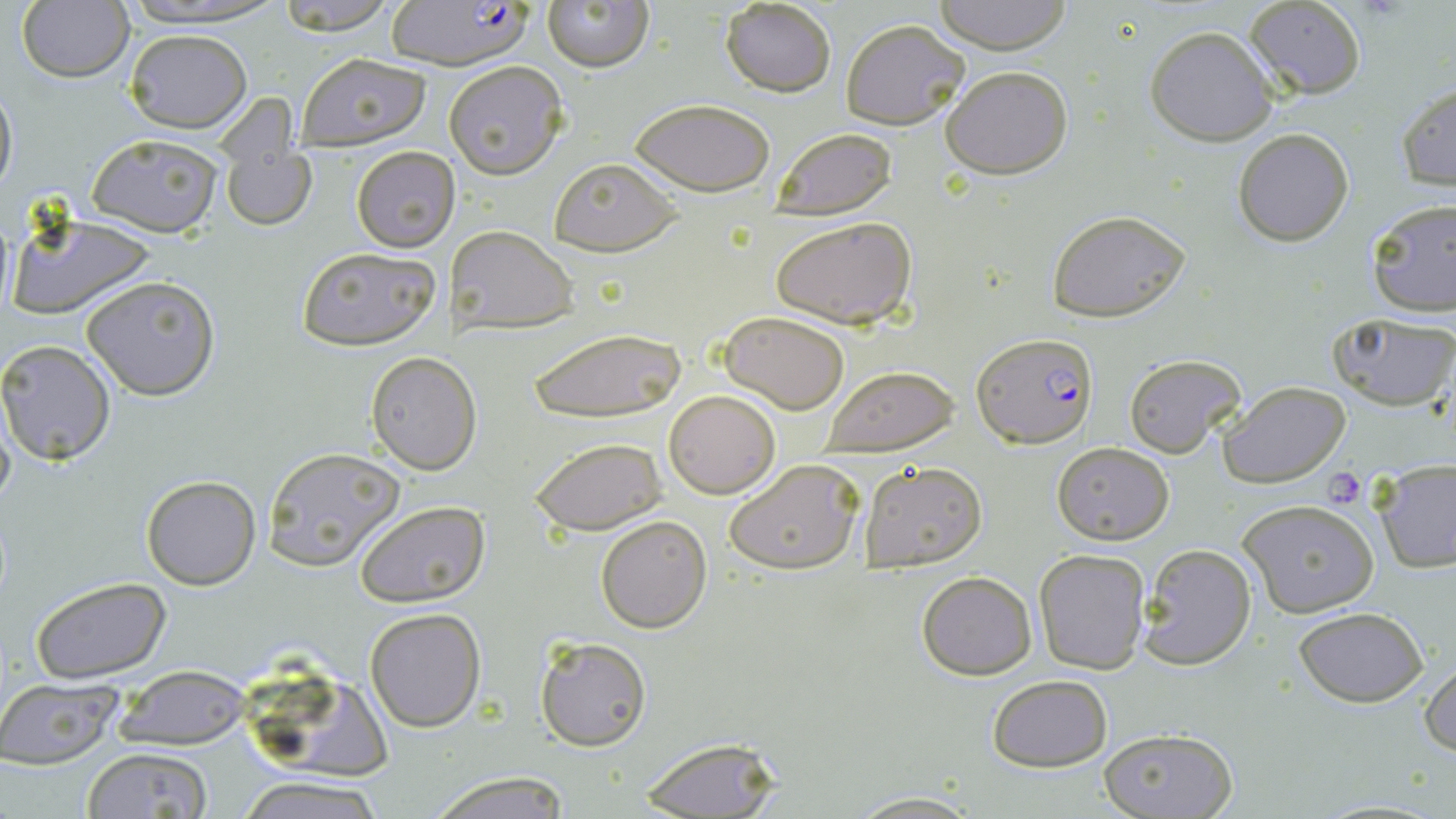

{
  "slide_level_diagnosis": "Plasmodium falciparum",
  "magnification": "1000x",
  "modality": "optical microscopy",
  "plasmodium_falciparum_infected_red_blood_cell_locations": "approximate bounding boxes as (x1,y1)-(x2,y2) corner pairs in pixels: (379,1)-(537,70), (973,332)-(1098,449)",
  "stain": "May-Grünwald-Giemsa",
  "uninfected_red_blood_cell_locations": "approximate bounding boxes as (x1,y1)-(x2,y2) corner pairs in pixels: (113,0)-(288,27), (272,0)-(399,35), (933,0)-(1074,54), (1242,0)-(1368,99), (16,1)-(135,85), (541,1)-(653,72), (718,1)-(837,96), (840,18)-(970,129), (1143,25)-(1280,147), (124,29)-(251,132), (295,51)-(432,152), (443,61)-(569,180), (940,64)-(1073,180), (0,77)-(18,201), (1395,82)-(1455,192), (628,98)-(775,196), (216,111)-(317,233), (771,127)-(897,220), (1232,129)-(1355,246), (85,133)-(224,238), (351,145)-(461,253), (548,157)-(682,257), (1365,198)-(1455,318), (1045,209)-(1193,322), (5,213)-(159,322), (770,214)-(919,330), (447,226)-(578,335), (294,246)-(442,351), (80,274)-(222,401), (720,311)-(850,413), (1329,313)-(1456,412), (526,326)-(687,422), (0,340)-(118,465), (366,352)-(480,474), (1123,353)-(1247,458), (819,365)-(961,456), (1217,381)-(1350,487), (664,390)-(780,498), (531,437)-(667,535), (1052,442)-(1174,545), (261,446)-(406,572), (722,459)-(863,574), (859,461)-(987,572), (1372,461)-(1456,572), (141,474)-(262,591), (1237,497)-(1382,620), (355,501)-(491,607), (595,515)-(711,633), (1137,543)-(1258,671), (1033,548)-(1151,674), (916,571)-(1037,679), (28,577)-(172,684), (366,607)-(486,732), (1294,608)-(1428,707), (535,636)-(650,750), (1420,657)-(1456,761), (107,671)-(248,749), (986,674)-(1113,771), (0,679)-(125,769), (264,684)-(393,781), (1098,727)-(1239,819), (637,736)-(784,817), (80,748)-(215,819), (424,770)-(575,817), (233,775)-(389,819), (845,791)-(984,818)",
  "platelet_locations": "approximate bounding boxes as (x1,y1)-(x2,y2) corner pairs in pixels: (1321,467)-(1367,508)",
  "preparation": "thin blood film",
  "field_of_view": "single",
  "image_size": "1456×819 pixels"
}